Assess this cell for malaria.
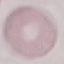
Uninfected.

Summary:
  - Capture: smartphone camera at the microscope eyepiece
  - Image type: cell patch, automatically extracted from a larger field of view and resized to 64 × 64 pixels
  - Stain: Giemsa
  - Preparation: thin blood smear